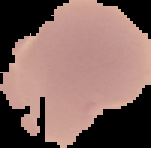

Summary:
  - Image type: segmented cell region with the area outside set to black
  - Malaria status: uninfected
  - Image size: 151×148 pixels
  - Preparation: thin blood smear